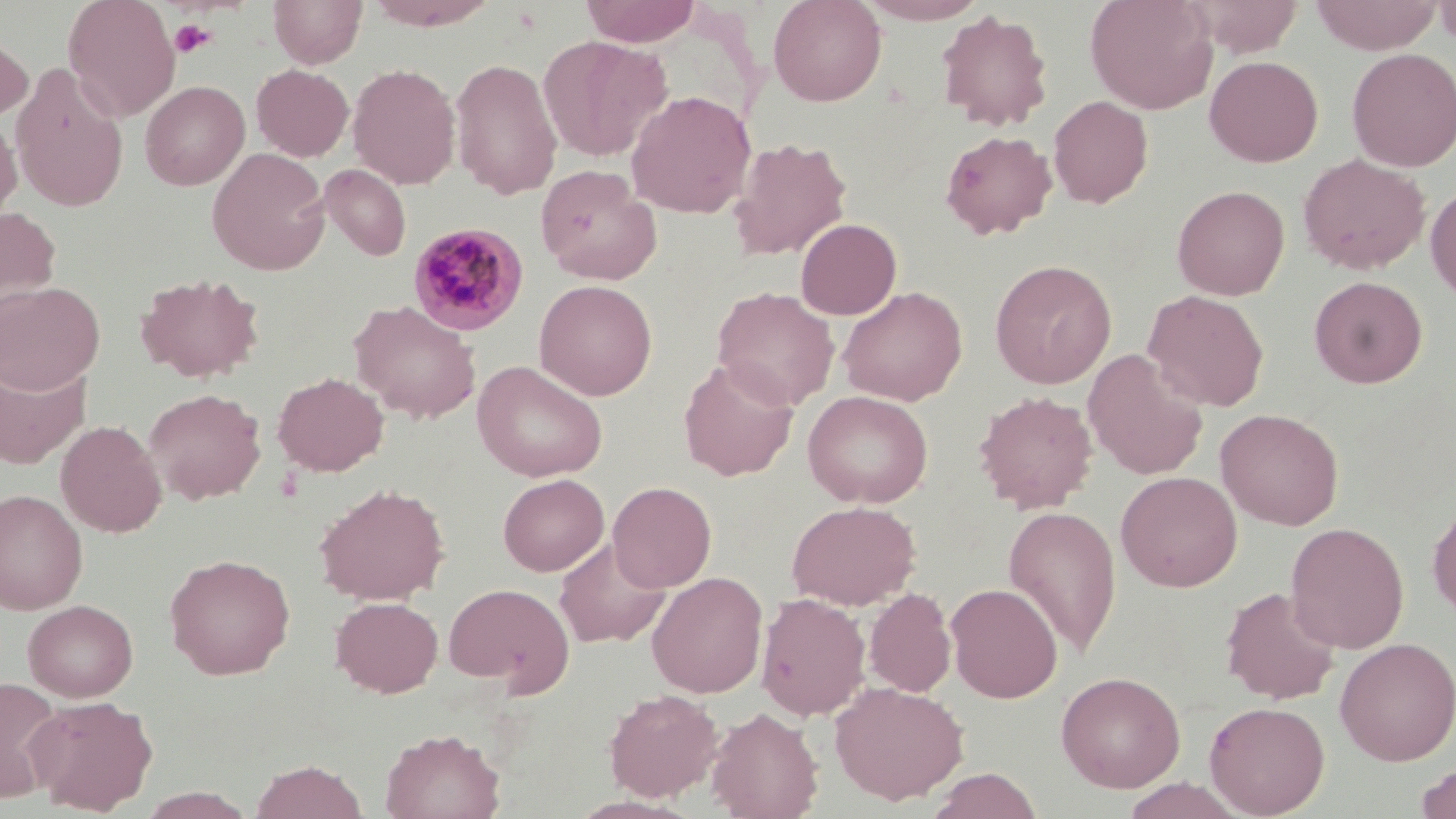
Summary:
  - Coordinate format: approximate bounding boxes as [x1, y1, x2, y2] in pixels
  - Plasmodium malariae-infected red blood cell locations: [407, 221, 529, 334]
  - Uninfected red blood cell locations: [63, 0, 181, 121], [268, 0, 368, 68], [364, 0, 500, 30], [581, 0, 701, 46], [768, 0, 887, 106], [854, 0, 989, 24], [1085, 0, 1218, 115], [1189, 0, 1303, 57], [1310, 0, 1442, 54], [1434, 0, 1456, 49], [935, 9, 1054, 132], [0, 31, 33, 124], [538, 35, 672, 162], [1346, 48, 1456, 172], [1204, 55, 1323, 167], [450, 57, 563, 200], [10, 62, 129, 212], [348, 63, 461, 189], [251, 64, 354, 161], [140, 80, 250, 190], [625, 89, 757, 219], [1049, 95, 1153, 208], [0, 113, 21, 224], [940, 130, 1056, 239], [727, 137, 851, 262], [207, 147, 331, 275], [1298, 153, 1430, 274], [319, 164, 411, 261], [535, 164, 661, 285], [1425, 181, 1456, 303], [1171, 185, 1290, 300], [0, 206, 61, 318], [796, 218, 902, 320], [990, 259, 1116, 389], [134, 271, 264, 383], [1309, 275, 1427, 388], [534, 279, 657, 400], [0, 282, 104, 395], [838, 286, 967, 406], [713, 287, 839, 410], [1143, 290, 1269, 412], [349, 300, 481, 423], [1083, 349, 1208, 481], [0, 357, 90, 469], [679, 357, 799, 482], [473, 361, 608, 482], [272, 371, 389, 476], [144, 388, 266, 503], [802, 390, 934, 508], [973, 390, 1098, 513], [1215, 407, 1344, 530], [56, 419, 167, 537], [1116, 471, 1242, 592], [498, 473, 609, 576], [608, 481, 716, 592], [314, 482, 450, 605], [0, 489, 88, 615], [1428, 498, 1456, 623], [787, 500, 921, 609], [1003, 505, 1122, 656], [1285, 522, 1409, 654], [554, 538, 671, 648], [164, 553, 296, 680], [647, 571, 767, 698], [945, 583, 1063, 703], [443, 584, 574, 692], [1220, 586, 1341, 705], [864, 588, 957, 697], [756, 593, 870, 721], [330, 596, 443, 697], [22, 599, 138, 702], [1334, 637, 1456, 765], [1056, 670, 1185, 792], [0, 676, 65, 802], [829, 680, 968, 805], [603, 688, 722, 801], [26, 695, 158, 815], [1204, 700, 1330, 817], [706, 706, 824, 819], [380, 728, 506, 819], [249, 759, 367, 819], [1415, 763, 1456, 819], [925, 768, 1043, 818], [1118, 777, 1249, 819], [136, 788, 257, 819]
  - Platelet locations: [169, 18, 216, 58]
  - Slide-level diagnosis: Plasmodium malariae
  - Modality: optical microscopy
  - Preparation: thin blood film
  - Field of view: single
  - Image size: 1456×819 pixels
  - Magnification: 1000x
  - Stain: May-Grünwald-Giemsa